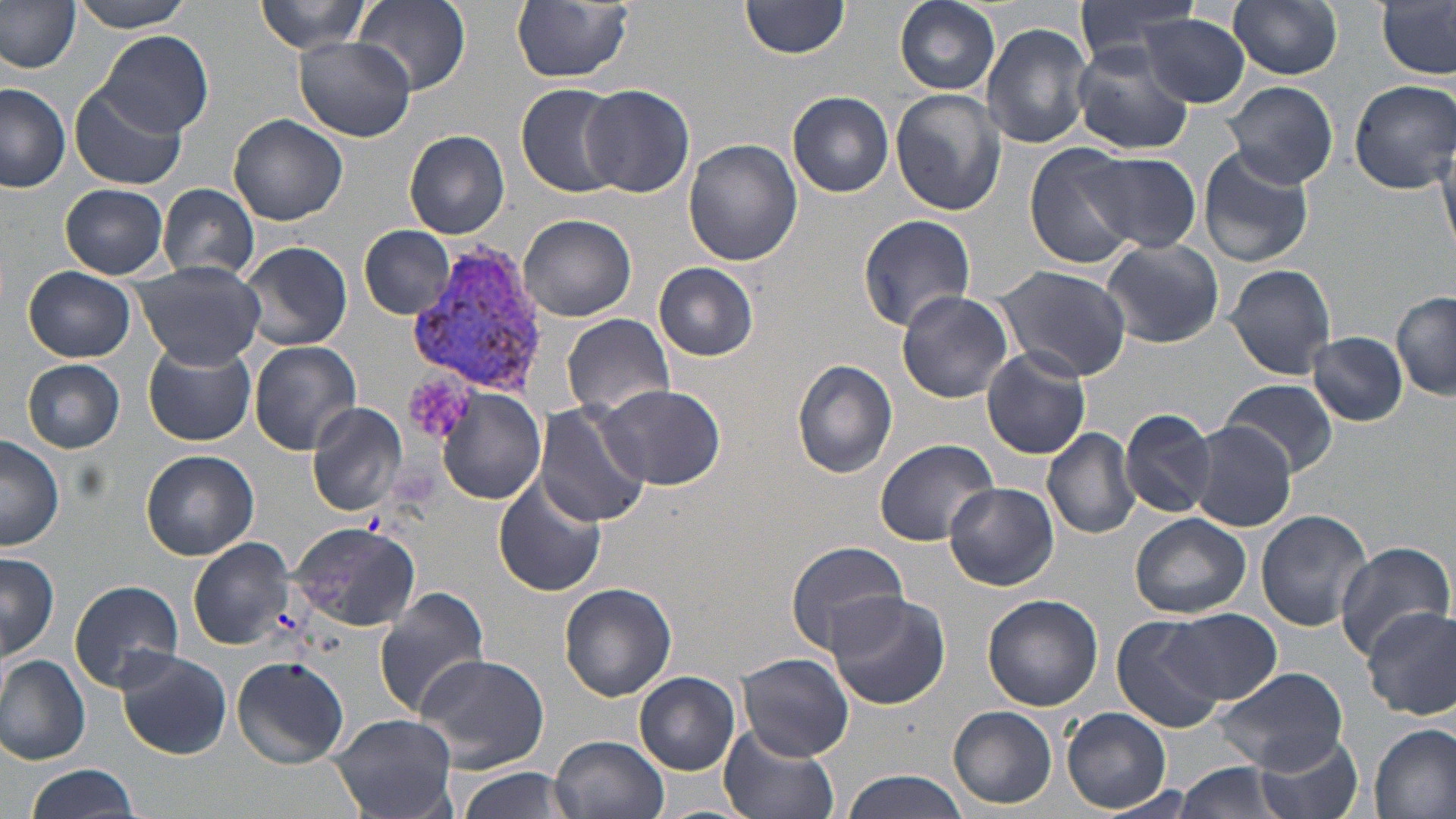

Approximate bounding boxes as [x1, y1, x2, y2] in pixels. Plasmodium vivax-infected red blood cell locations: [411, 242, 553, 400]. Uninfected red blood cell locations: [71, 0, 199, 32], [253, 0, 372, 55], [354, 0, 470, 95], [741, 0, 852, 58], [894, 0, 1003, 96], [1074, 0, 1204, 66], [1228, 0, 1344, 81], [1376, 0, 1455, 78], [510, 1, 633, 83], [0, 4, 80, 72], [1139, 15, 1251, 106], [982, 23, 1094, 150], [99, 30, 212, 139], [296, 37, 413, 141], [1071, 43, 1194, 154], [1348, 79, 1455, 193], [1225, 80, 1338, 190], [69, 83, 188, 191], [516, 84, 624, 198], [580, 84, 694, 198], [0, 85, 71, 193], [889, 89, 1006, 217], [788, 91, 895, 198], [228, 113, 349, 226], [404, 130, 512, 239], [1431, 133, 1455, 256], [683, 137, 801, 266], [1023, 143, 1141, 268], [1197, 145, 1316, 269], [1078, 151, 1202, 254], [60, 184, 170, 279], [156, 184, 261, 281], [855, 212, 977, 333], [520, 214, 637, 322], [359, 224, 456, 320], [1099, 238, 1225, 348], [237, 240, 352, 351], [132, 260, 265, 370], [654, 262, 760, 361], [988, 264, 1134, 383], [1225, 264, 1337, 381], [24, 265, 136, 362], [896, 290, 1015, 403], [1391, 290, 1456, 401], [563, 314, 673, 417], [1309, 331, 1407, 427], [250, 341, 362, 454], [143, 344, 256, 446], [981, 347, 1093, 459], [22, 358, 126, 453], [792, 359, 897, 477], [1221, 377, 1338, 477], [596, 383, 725, 491], [439, 389, 545, 505], [306, 401, 407, 517], [534, 403, 650, 529], [1120, 406, 1217, 519], [1188, 422, 1298, 533], [1042, 426, 1140, 539], [0, 436, 65, 550], [873, 437, 999, 546], [142, 450, 258, 560], [493, 476, 607, 597], [945, 483, 1059, 590], [1256, 509, 1374, 631], [1131, 513, 1251, 618], [290, 522, 422, 634], [189, 537, 297, 650], [784, 541, 911, 653], [1334, 542, 1454, 662], [0, 551, 59, 662], [69, 579, 186, 692], [560, 582, 677, 700], [373, 585, 490, 721], [824, 590, 951, 710], [983, 595, 1101, 711], [1363, 606, 1456, 721], [1161, 609, 1279, 705], [1112, 614, 1227, 735], [116, 648, 232, 760], [738, 654, 853, 760], [416, 655, 553, 771], [0, 656, 92, 765], [231, 656, 350, 767], [1207, 666, 1348, 774], [636, 673, 739, 774], [949, 706, 1058, 809], [1062, 707, 1173, 812], [329, 713, 457, 817], [1370, 722, 1456, 819], [719, 726, 839, 819], [1253, 731, 1363, 819], [551, 734, 670, 819], [1171, 762, 1291, 819], [22, 766, 143, 819], [453, 767, 573, 819], [838, 769, 975, 819]. Platelet locations: [407, 374, 475, 438]. Slide-level diagnosis: Plasmodium vivax. Light microscopy. Captured at 1000x magnification. Thin blood smear. May-Grünwald-Giemsa-stained preparation. Single field of view. Image is 1456×819 pixels.